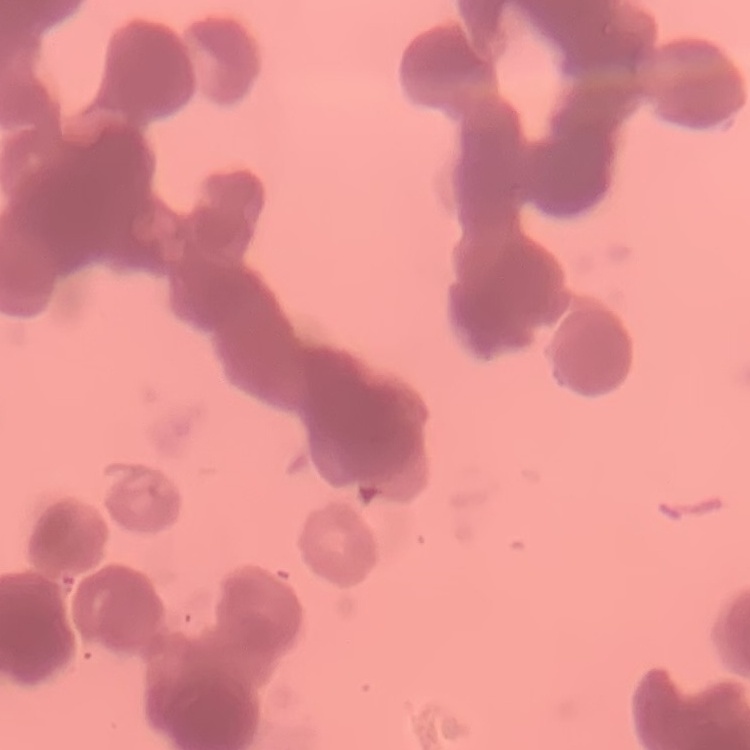

The red blood cells show rouleaux formation. Stained with either Field's or Giemsa. One tile cut from a larger photomicrograph. Thin peripheral smear.